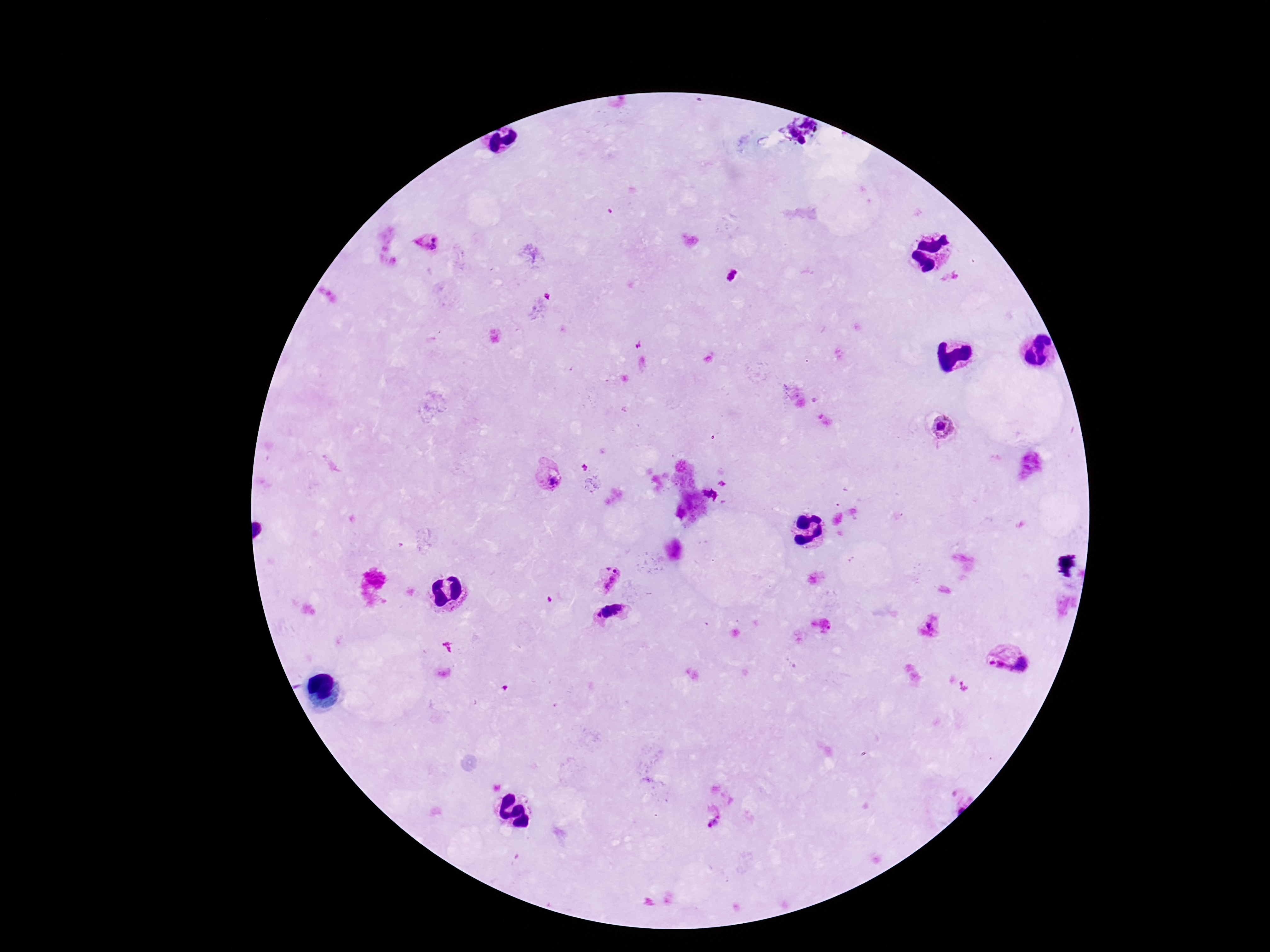

Approximate centers as [x, y] in pixels.
Summary:
  - Plasmodium parasite locations: [808, 123], [792, 133], [801, 141], [434, 239], [432, 247], [732, 275], [945, 428], [550, 480], [610, 578], [611, 613], [929, 625], [1025, 662], [999, 667], [716, 820]
  - Field of view: single
  - Capture: smartphone camera through the microscope eyepiece
  - Stain: Giemsa
  - Image size: 1270×952 pixels
  - Patient malaria status: infected
  - Preparation: thick blood film
  - Magnification: 100x